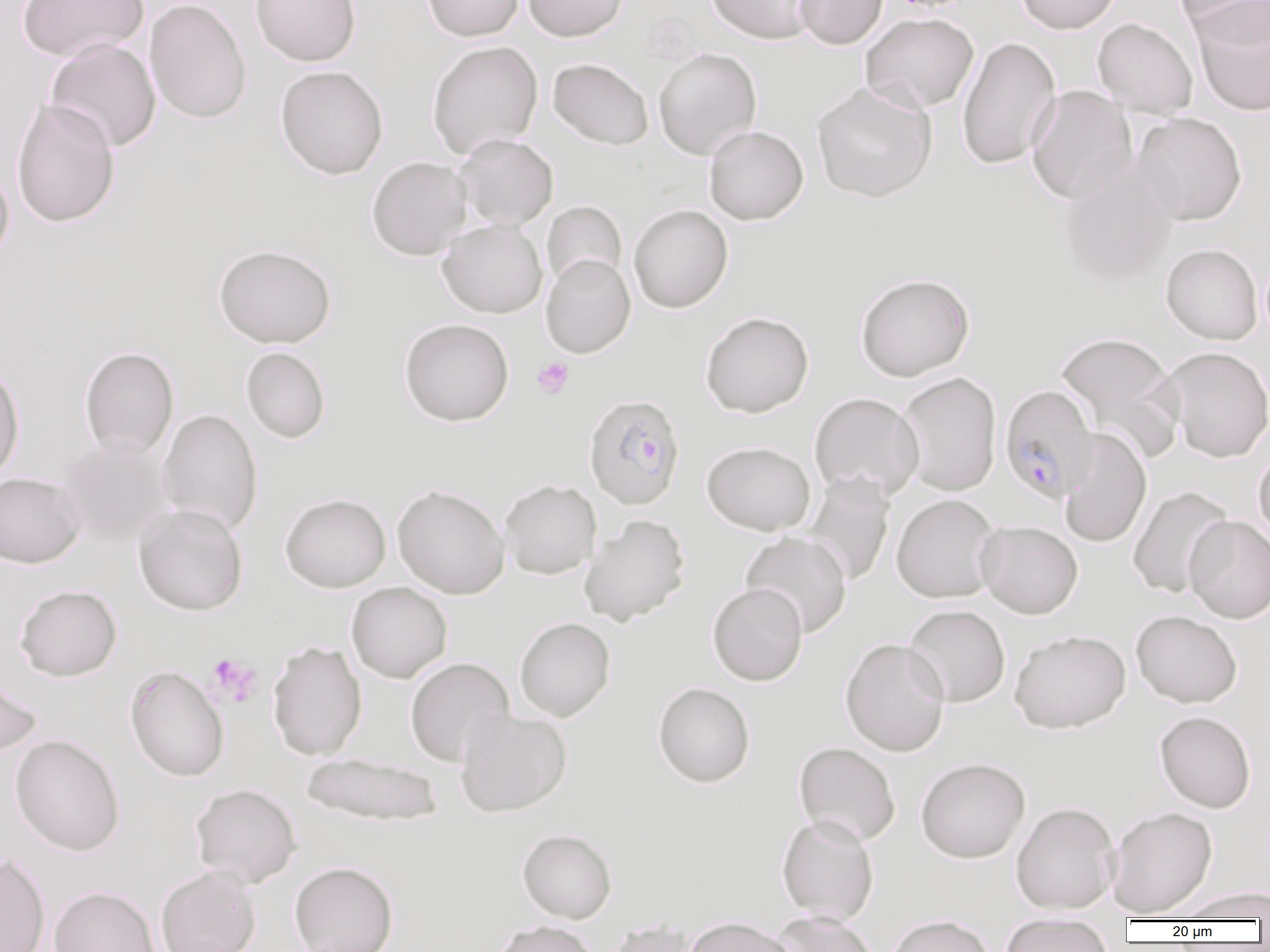

Summary:
  - Coordinate format: approximate bounding boxes as named x1/y1/x2/y2 corners in pixels
  - Platelet locations: (x1=532, y1=357, x2=574, y2=398), (x1=206, y1=654, x2=262, y2=707)
  - Plasmodium falciparum-infected red blood cell locations: (x1=1000, y1=384, x2=1100, y2=502), (x1=583, y1=394, x2=685, y2=509)
  - Uninfected red blood cell locations: (x1=18, y1=0, x2=149, y2=62), (x1=145, y1=0, x2=251, y2=125), (x1=249, y1=0, x2=361, y2=66), (x1=422, y1=0, x2=524, y2=41), (x1=522, y1=0, x2=629, y2=42), (x1=706, y1=0, x2=819, y2=45), (x1=793, y1=0, x2=888, y2=49), (x1=1014, y1=0, x2=1123, y2=34), (x1=1179, y1=0, x2=1270, y2=50), (x1=1192, y1=4, x2=1270, y2=116), (x1=860, y1=12, x2=979, y2=113), (x1=1092, y1=18, x2=1198, y2=118), (x1=956, y1=36, x2=1061, y2=169), (x1=45, y1=37, x2=161, y2=152), (x1=426, y1=40, x2=543, y2=159), (x1=653, y1=47, x2=762, y2=160), (x1=548, y1=58, x2=654, y2=150), (x1=275, y1=65, x2=388, y2=180), (x1=812, y1=82, x2=937, y2=203), (x1=1026, y1=86, x2=1138, y2=205), (x1=11, y1=98, x2=120, y2=228), (x1=1131, y1=112, x2=1248, y2=226), (x1=704, y1=125, x2=808, y2=224), (x1=454, y1=134, x2=558, y2=230), (x1=367, y1=156, x2=471, y2=261), (x1=1058, y1=160, x2=1178, y2=287), (x1=0, y1=161, x2=14, y2=268), (x1=542, y1=201, x2=627, y2=290), (x1=629, y1=204, x2=733, y2=313), (x1=437, y1=219, x2=547, y2=318), (x1=213, y1=243, x2=336, y2=348), (x1=1161, y1=243, x2=1263, y2=345), (x1=541, y1=254, x2=635, y2=358), (x1=854, y1=273, x2=975, y2=381), (x1=700, y1=311, x2=814, y2=417), (x1=399, y1=318, x2=514, y2=426), (x1=1055, y1=331, x2=1185, y2=463), (x1=79, y1=346, x2=179, y2=459), (x1=1161, y1=346, x2=1270, y2=462), (x1=241, y1=347, x2=330, y2=443), (x1=0, y1=364, x2=25, y2=482), (x1=895, y1=372, x2=1002, y2=496), (x1=809, y1=392, x2=925, y2=502), (x1=157, y1=408, x2=263, y2=534), (x1=1057, y1=428, x2=1152, y2=548), (x1=57, y1=436, x2=174, y2=547), (x1=702, y1=441, x2=815, y2=535), (x1=1253, y1=442, x2=1270, y2=546), (x1=803, y1=471, x2=895, y2=586), (x1=0, y1=472, x2=86, y2=568), (x1=499, y1=479, x2=602, y2=579), (x1=392, y1=484, x2=510, y2=599), (x1=1127, y1=486, x2=1234, y2=598), (x1=280, y1=493, x2=391, y2=592), (x1=891, y1=494, x2=1002, y2=603), (x1=133, y1=503, x2=248, y2=615), (x1=579, y1=514, x2=690, y2=625), (x1=1184, y1=515, x2=1270, y2=623), (x1=975, y1=520, x2=1083, y2=619), (x1=740, y1=531, x2=852, y2=638), (x1=346, y1=582, x2=452, y2=683), (x1=707, y1=582, x2=807, y2=685), (x1=14, y1=584, x2=122, y2=681), (x1=903, y1=604, x2=1010, y2=707), (x1=1131, y1=610, x2=1243, y2=708), (x1=514, y1=617, x2=615, y2=721), (x1=1009, y1=629, x2=1131, y2=733), (x1=840, y1=637, x2=950, y2=757), (x1=267, y1=640, x2=367, y2=761), (x1=405, y1=657, x2=514, y2=766), (x1=124, y1=665, x2=230, y2=782), (x1=0, y1=669, x2=42, y2=759), (x1=653, y1=682, x2=755, y2=787), (x1=455, y1=709, x2=572, y2=816), (x1=1155, y1=711, x2=1256, y2=812), (x1=9, y1=734, x2=125, y2=856), (x1=793, y1=742, x2=901, y2=846), (x1=300, y1=753, x2=443, y2=826), (x1=915, y1=757, x2=1030, y2=863), (x1=190, y1=783, x2=302, y2=888), (x1=1010, y1=801, x2=1121, y2=914), (x1=1107, y1=806, x2=1217, y2=917), (x1=776, y1=814, x2=879, y2=925), (x1=517, y1=829, x2=617, y2=923), (x1=0, y1=853, x2=50, y2=952), (x1=289, y1=861, x2=399, y2=952), (x1=155, y1=864, x2=261, y2=952), (x1=49, y1=885, x2=160, y2=952), (x1=1175, y1=887, x2=1270, y2=921), (x1=771, y1=910, x2=880, y2=952), (x1=1000, y1=912, x2=1113, y2=952), (x1=885, y1=914, x2=996, y2=952), (x1=683, y1=916, x2=799, y2=952), (x1=491, y1=920, x2=600, y2=952), (x1=603, y1=920, x2=699, y2=952)
  - Slide-level diagnosis: Plasmodium falciparum
  - Field of view: single
  - Image size: 1270×952 pixels
  - Preparation: thin blood smear
  - Modality: optical microscopy
  - Magnification: 1000x